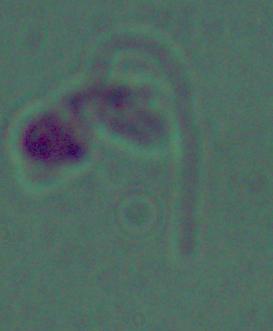
Photomicrograph. A Leishmania parasite is seen. 1000x magnification.